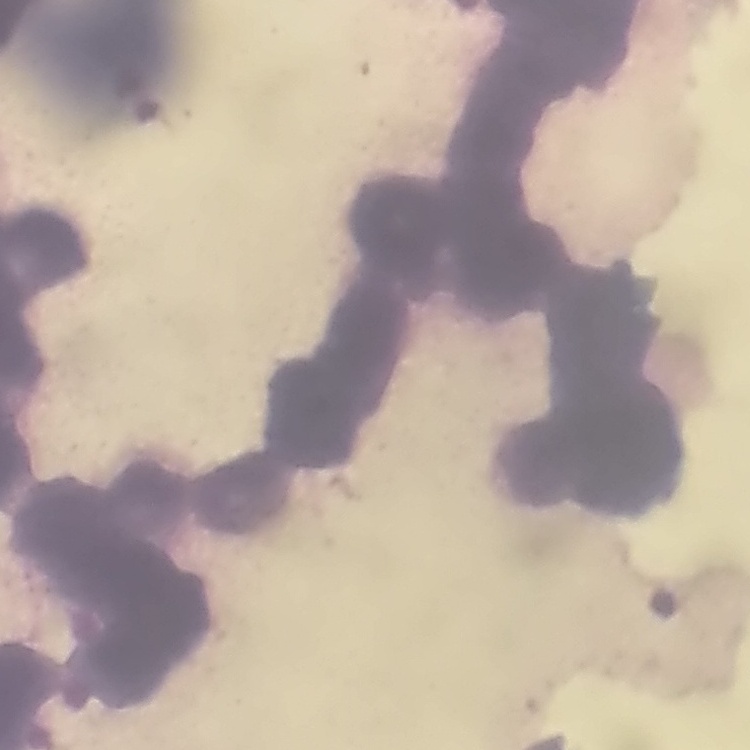
The erythrocytes exhibit rouleaux formation. Stained with either Field's or Giemsa. One tile cut from a larger photomicrograph. Thin blood smear.